Locate every blood parasite and identify its species.
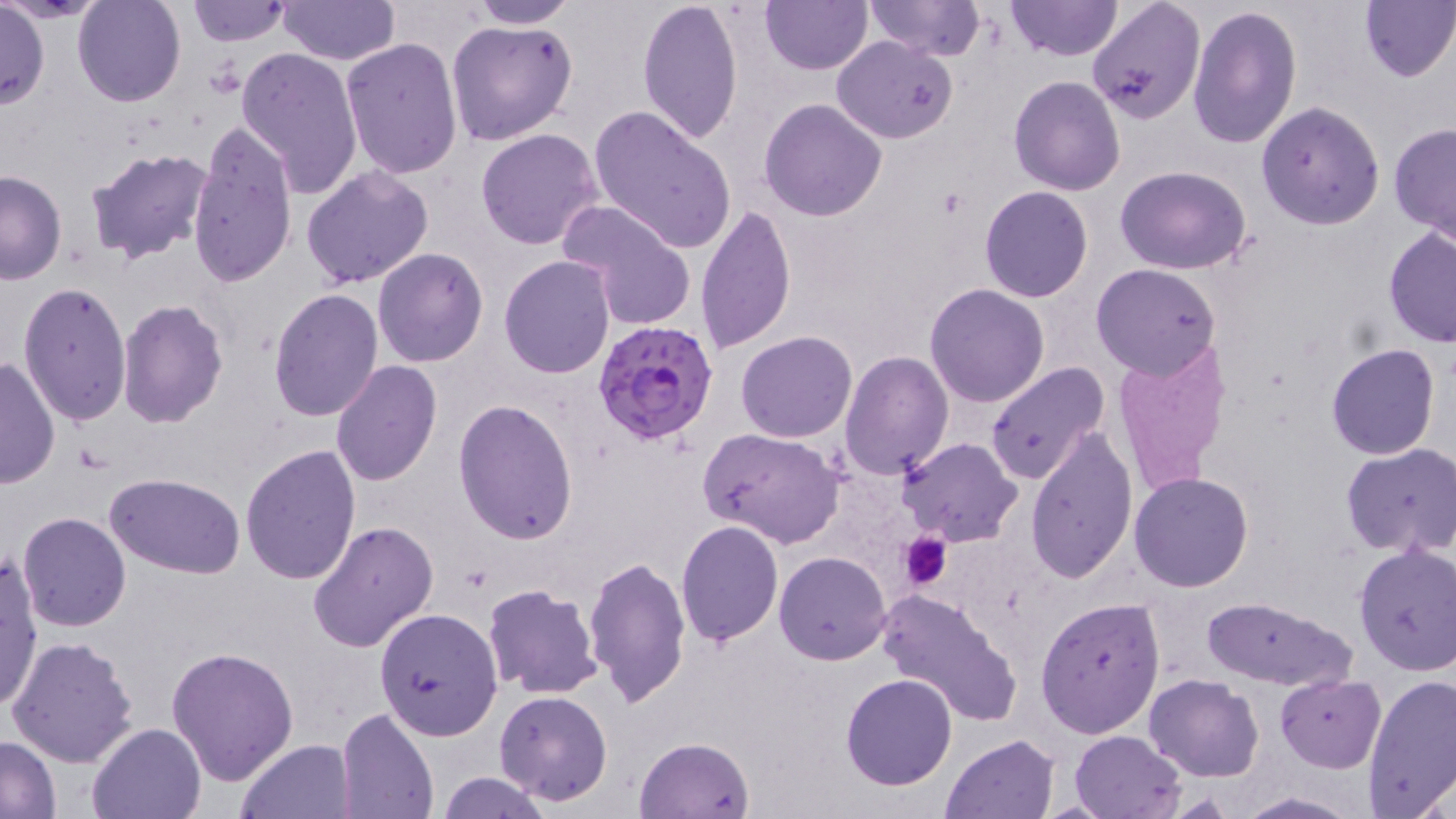

Approximate bounding boxes as (x1, y1, x2, y2) in pixels.
Plasmodium falciparum-infected red blood cells: (593, 318, 720, 448).
No Plasmodium ovale, Plasmodium malariae, Plasmodium vivax, Babesia divergens, or Trypanosoma brucei observed.

Summary:
  - Uninfected red blood cell locations: (73, 0, 186, 107), (185, 0, 290, 46), (279, 0, 400, 65), (463, 0, 578, 28), (635, 0, 744, 145), (759, 0, 871, 74), (863, 0, 984, 63), (1006, 0, 1123, 62), (1088, 0, 1207, 125), (1358, 0, 1456, 82), (0, 1, 47, 110), (1187, 3, 1302, 150), (446, 18, 578, 145), (832, 36, 958, 142), (341, 37, 464, 180), (235, 47, 364, 198), (1009, 75, 1125, 194), (758, 98, 886, 222), (1256, 101, 1385, 230), (589, 104, 737, 254), (1389, 121, 1456, 243), (186, 123, 297, 290), (476, 127, 603, 250), (85, 145, 216, 266), (301, 164, 434, 289), (1117, 166, 1252, 274), (0, 170, 67, 284), (979, 185, 1093, 303), (559, 201, 696, 331), (695, 203, 796, 354), (1383, 225, 1456, 348), (372, 248, 489, 367), (498, 255, 615, 377), (1091, 263, 1221, 381), (17, 281, 133, 427), (925, 283, 1050, 407), (267, 288, 384, 423), (117, 299, 229, 428), (735, 331, 856, 443), (1111, 340, 1235, 499), (1326, 343, 1439, 461), (841, 350, 953, 480), (0, 356, 60, 489), (330, 361, 442, 486), (984, 362, 1109, 485), (454, 399, 580, 545), (700, 427, 845, 548), (1025, 427, 1138, 584), (898, 438, 1022, 548), (240, 442, 362, 584), (1341, 442, 1456, 558), (1130, 471, 1255, 592), (105, 472, 247, 579), (16, 512, 132, 632), (308, 518, 440, 653), (676, 518, 785, 647), (1353, 543, 1456, 676), (774, 549, 892, 664), (1, 553, 43, 712), (584, 553, 690, 709), (482, 584, 601, 701), (876, 587, 1023, 728), (1200, 595, 1357, 690), (1036, 597, 1165, 740), (374, 606, 503, 740), (6, 634, 137, 769), (166, 644, 298, 785), (1361, 672, 1456, 817), (840, 673, 958, 791), (1145, 674, 1264, 782), (1276, 674, 1385, 771), (493, 689, 614, 806), (336, 708, 439, 819), (88, 722, 206, 818), (1069, 730, 1185, 818), (941, 732, 1060, 817), (0, 736, 61, 817), (634, 736, 754, 818), (236, 737, 357, 819), (436, 771, 551, 818), (1236, 792, 1359, 818)
  - Platelet locations: (899, 532, 952, 589)
  - Slide-level diagnosis: Plasmodium falciparum
  - Preparation: thin blood film
  - Field of view: one of a larger specimen
  - Image size: 1456×819 pixels
  - Modality: light microscopy
  - Magnification: 1000x
  - Stain: May-Grünwald-Giemsa